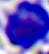

Summary:
  - Modality: micrograph
  - Identification: white blood cell
  - Magnification: 400x